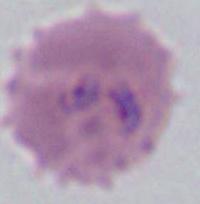

magnification: 400x or 1000x
identification: Plasmodium
modality: photomicrograph